Locate every blood parasite and identify its species.
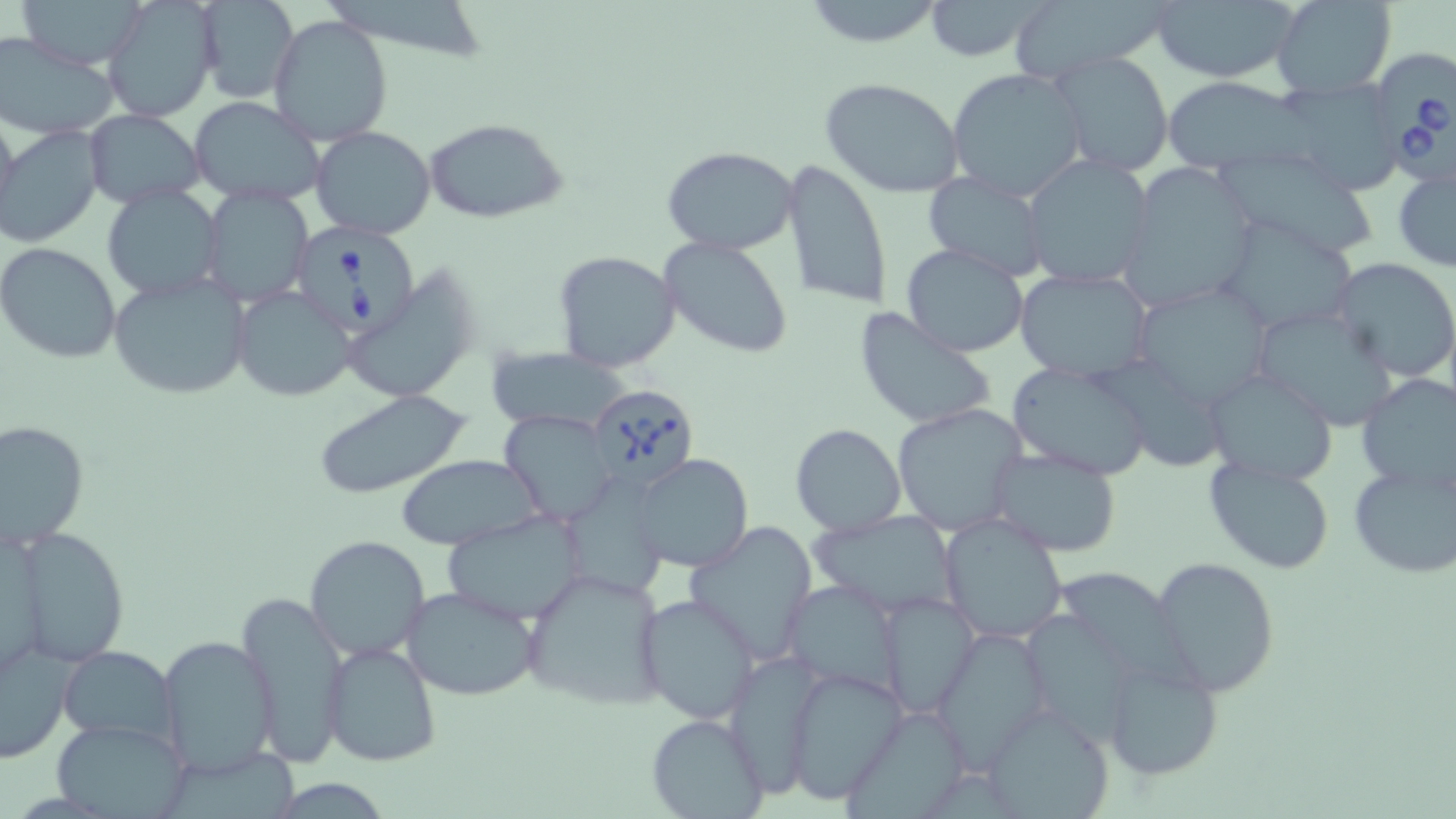
Approximate bounding boxes as [x1, y1, x2, y2] in pixels.
Babesia divergens-infected red blood cells: [1375, 50, 1456, 192], [293, 223, 428, 342], [587, 383, 700, 491].
No Plasmodium falciparum, Plasmodium ovale, Plasmodium malariae, Plasmodium vivax, or Trypanosoma brucei observed.

Uninfected red blood cell locations: [11, 0, 151, 69], [332, 0, 490, 77], [798, 0, 950, 48], [921, 0, 1055, 62], [1150, 0, 1301, 83], [1270, 0, 1397, 98], [194, 1, 299, 104], [1002, 1, 1174, 83], [101, 4, 218, 123], [267, 14, 393, 147], [0, 33, 119, 140], [1051, 51, 1174, 177], [947, 67, 1088, 202], [1162, 75, 1308, 172], [820, 76, 967, 199], [1272, 80, 1406, 195], [188, 95, 329, 206], [0, 103, 19, 235], [84, 109, 204, 208], [423, 118, 568, 223], [0, 123, 105, 248], [311, 126, 436, 240], [661, 144, 801, 256], [1218, 147, 1379, 260], [1020, 154, 1155, 289], [780, 156, 893, 313], [1118, 163, 1259, 315], [1392, 165, 1456, 271], [922, 171, 1051, 280], [101, 184, 225, 301], [202, 186, 316, 304], [1216, 216, 1359, 335], [658, 236, 796, 358], [1, 242, 121, 363], [900, 244, 1029, 357], [551, 251, 681, 374], [1330, 258, 1456, 383], [343, 267, 483, 406], [1013, 268, 1156, 382], [109, 272, 252, 401], [1131, 282, 1276, 411], [230, 286, 358, 402], [1250, 304, 1400, 431], [853, 309, 996, 432], [487, 348, 628, 434], [1007, 360, 1155, 481], [1103, 362, 1223, 481], [1202, 369, 1339, 486], [1355, 371, 1456, 494], [313, 388, 471, 500], [892, 402, 1028, 533], [499, 410, 618, 526], [0, 419, 88, 550], [790, 422, 907, 536], [989, 448, 1123, 558], [396, 453, 542, 551], [629, 453, 755, 574], [1203, 455, 1336, 574], [1347, 460, 1456, 578], [560, 478, 670, 601], [440, 508, 591, 625], [810, 508, 964, 618], [939, 513, 1067, 644], [684, 521, 818, 667], [15, 527, 132, 668], [304, 535, 431, 661], [1151, 556, 1280, 697], [518, 568, 669, 712], [1050, 569, 1196, 692], [785, 579, 905, 700], [400, 585, 541, 703], [235, 589, 350, 766], [879, 590, 976, 718], [637, 594, 762, 725], [1024, 611, 1151, 757], [928, 627, 1053, 767], [157, 636, 279, 779], [322, 640, 441, 767], [0, 644, 73, 764], [55, 646, 182, 749], [1097, 657, 1223, 783], [784, 665, 909, 802], [982, 704, 1115, 819], [841, 707, 971, 817], [646, 712, 766, 818], [50, 720, 191, 817], [171, 752, 308, 819], [285, 777, 402, 819]. Slide-level diagnosis: Babesia divergens. May-Grünwald-Giemsa-stained preparation. Image is 1456×819 pixels. One field of a larger specimen. Light microscopy. Captured at 1000x magnification. Thin blood film.